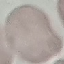
Summary:
  - Malaria status: uninfected
  - Stain: Giemsa
  - Capture: smartphone camera at the microscope eyepiece
  - Preparation: thin blood film
  - Image type: automatically extracted cell patch, resized to 64 × 64 pixels